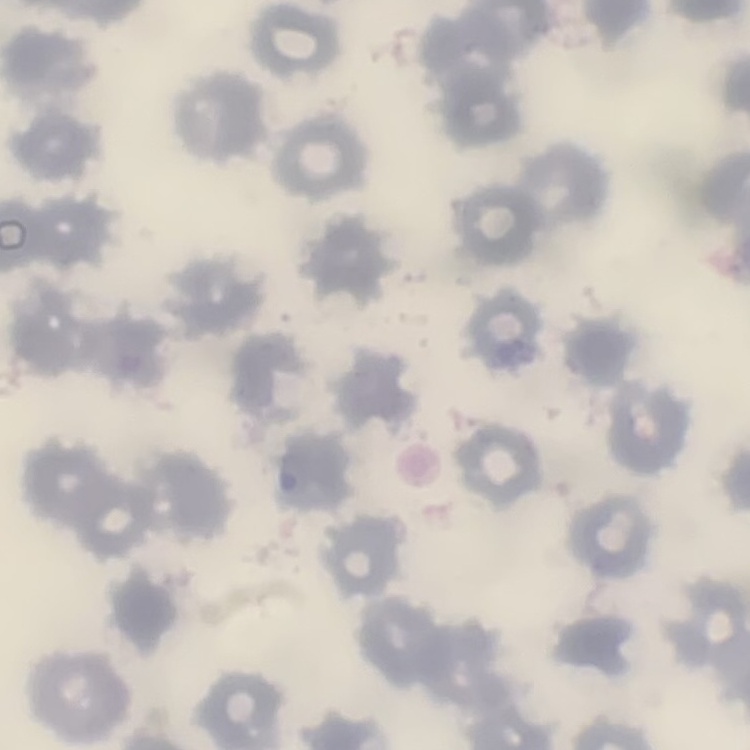
The red blood cells exhibit no rouleaux formation. Thin peripheral smear. Square crop of a larger photomicrograph. Field's or Giemsa stain.